Locate every malaria parasite.
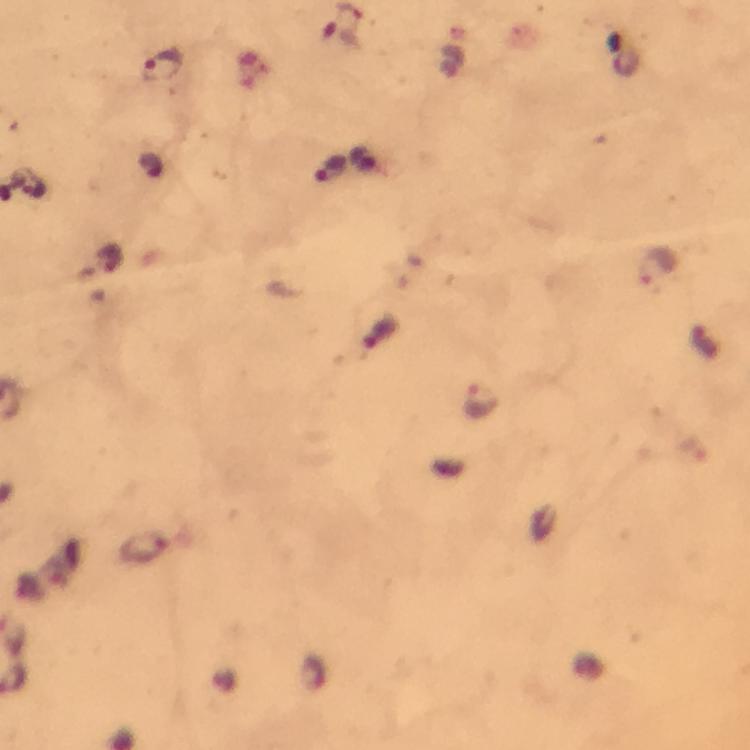
Approximate centers as {x, y} in pixels.
Malaria parasites: {163, 65}, {330, 168}, {113, 259}, {657, 266}, {481, 401}, {144, 548}.

cropped_from: a single field of view
magnification: 100x
preparation: thick smear
capture: smartphone photograph through a microscope
image_size: 750×750 pixels
stain: Giemsa
immersion_oil: applied
context: from a diagnostic examination for malaria